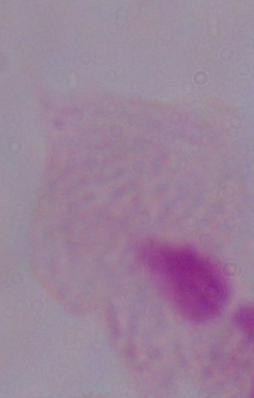 A trichomonad is seen. Photomicrograph. 1000x magnification.